Assess this cell for malaria.
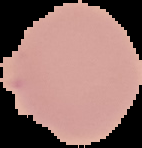

It is uninfected.

The area outside the segmented cell region is set to black. From a thin blood film. Image is 142×148 pixels.